Identify the cell.
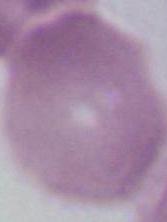
This is an erythrocyte.

Photomicrograph. Captured at 1000x magnification.